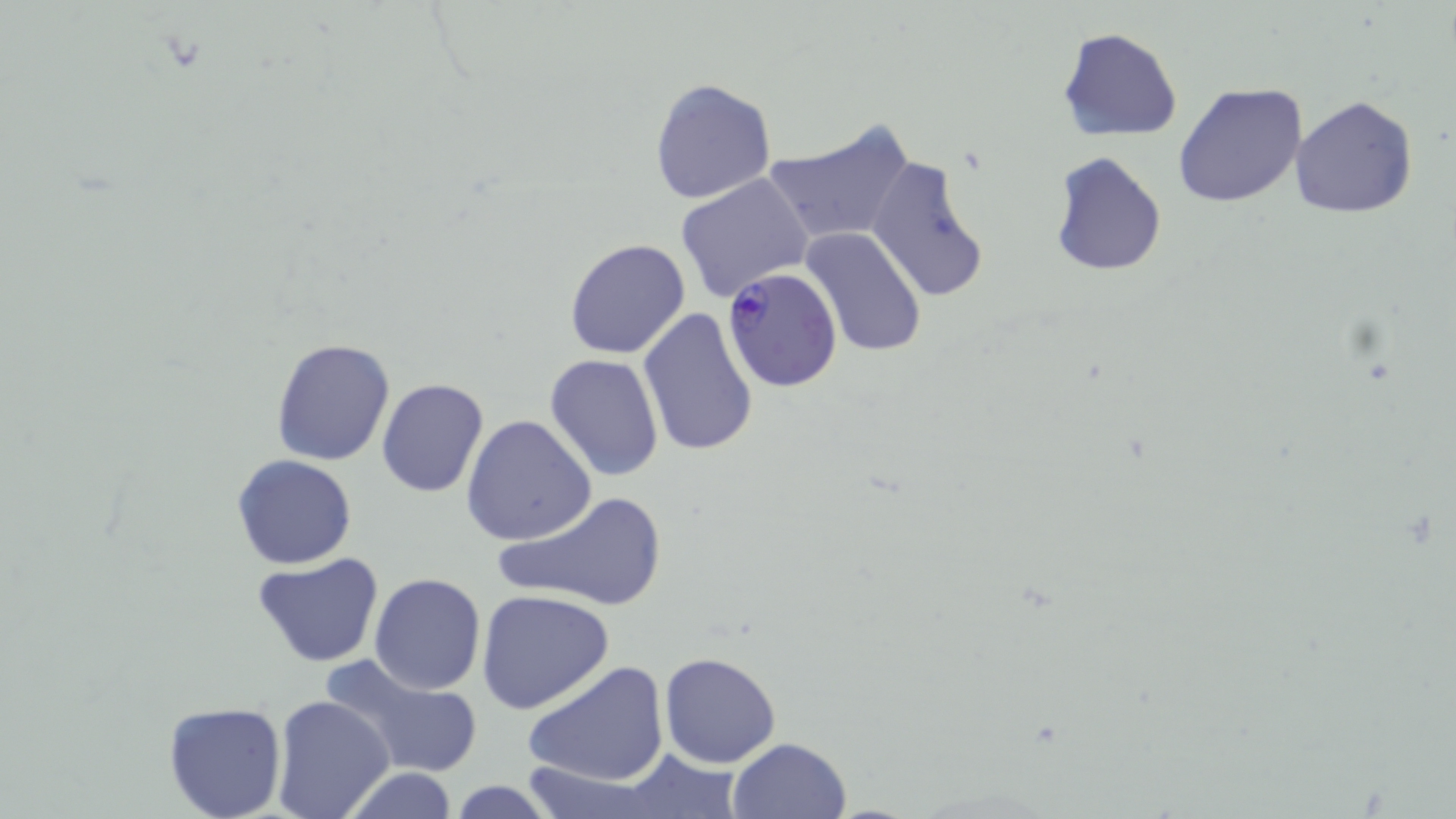
Summary:
  - Coordinate format: approximate bounding boxes as (x1,y1)-(x2,y2) corner pairs in pixels
  - Plasmodium falciparum-infected red blood cell locations: (723,266)-(843,393)
  - Uninfected red blood cell locations: (1058,27)-(1183,142), (649,76)-(778,205), (1174,82)-(1307,209), (1291,95)-(1420,219), (763,118)-(915,251), (1049,151)-(1167,277), (865,154)-(991,303), (676,173)-(814,304), (799,228)-(927,357), (565,236)-(692,359), (637,307)-(760,459), (270,336)-(396,466), (544,354)-(666,482), (376,378)-(488,498), (460,415)-(597,545), (231,454)-(358,570), (494,488)-(668,613), (251,554)-(385,668), (369,572)-(487,695), (476,590)-(617,716), (658,651)-(782,769), (319,653)-(485,780), (523,660)-(671,789), (271,695)-(395,819), (161,700)-(288,819), (727,737)-(852,819), (611,747)-(746,817), (519,763)-(660,819), (340,768)-(463,819), (443,780)-(560,818)
  - Slide-level diagnosis: Plasmodium falciparum
  - Image size: 1456×819 pixels
  - Stain: May-Grünwald-Giemsa
  - Preparation: thin blood film
  - Modality: optical microscopy
  - Field of view: one of a larger specimen
  - Magnification: 1000x